Identify the parasite.
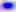

Toxoplasma gondii.

Summary:
  - Modality: micrograph
  - Magnification: 400x